Identify the parasite.
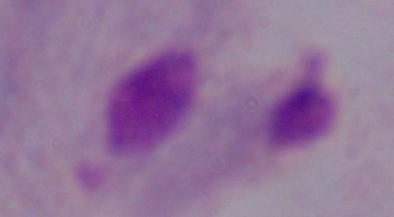

This is a trichomonad.

{
  "modality": "micrograph",
  "magnification": "1000x"
}